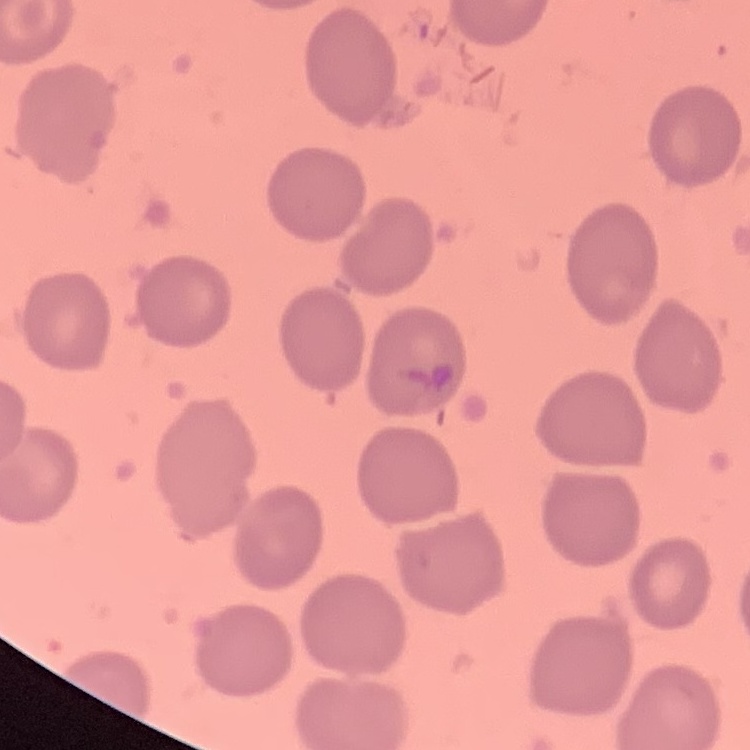
The erythrocytes show no rouleaux formation. Thin peripheral smear. One tile cut from a larger photomicrograph. Stained with either Field's or Giemsa.